Comment on the morphology of the red blood cells.
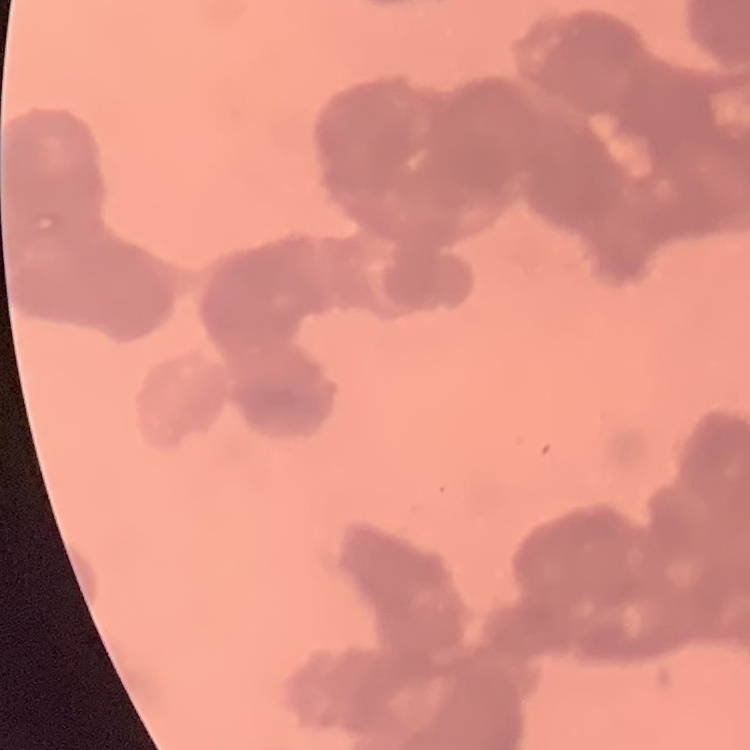

Rouleaux formation.

{
  "stain": "Field's or Giemsa",
  "preparation": "thin blood film",
  "image_type": "one tile cut from a larger photomicrograph"
}